Classify this cell by malaria status.
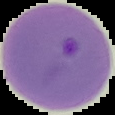
It is parasitized.

Image is 115×115 pixels. The area outside the segmented cell region is set to black. From a thin blood smear.